Name the blood parasite species.
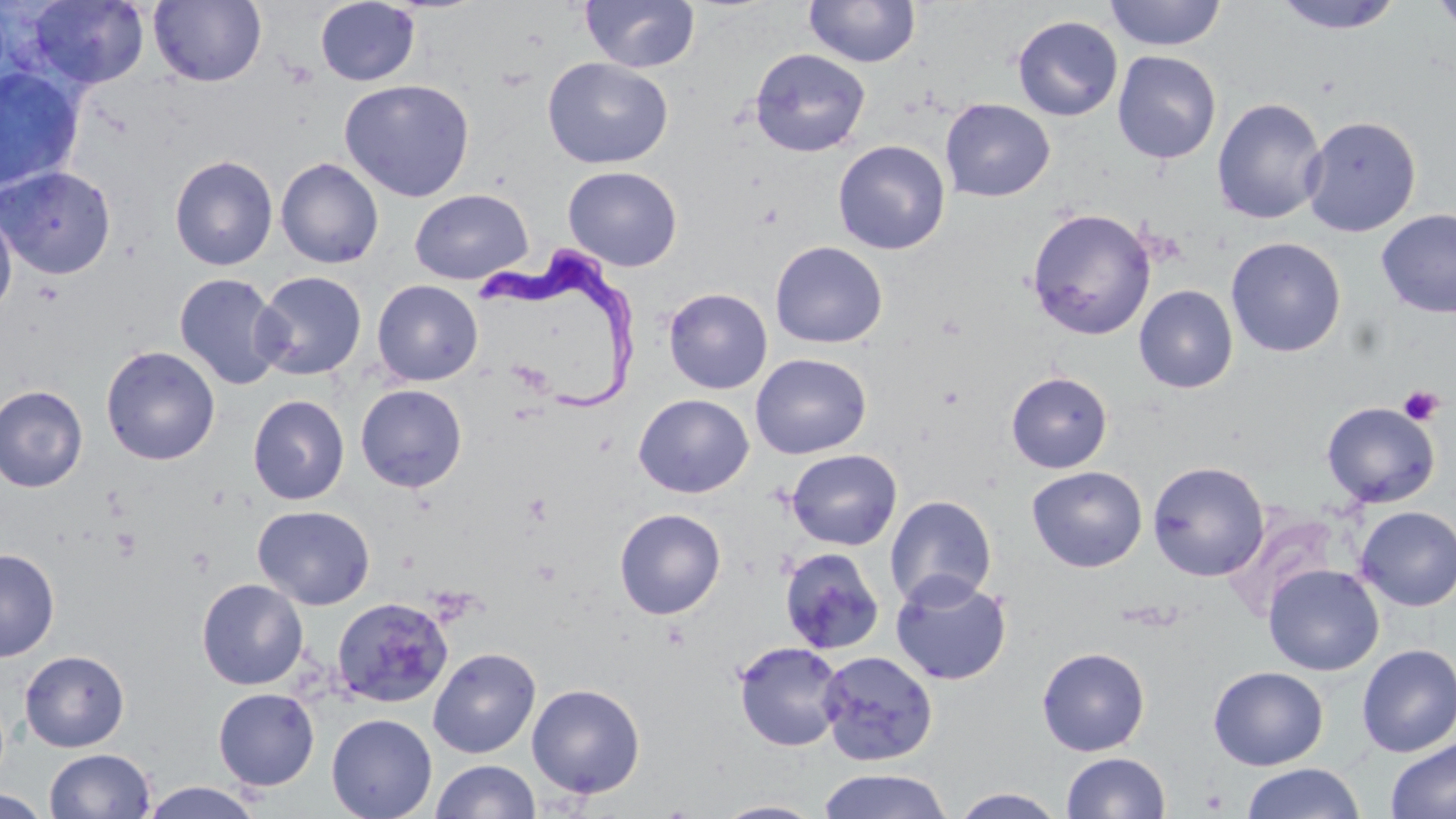
Trypanosoma brucei.

Approximate bounding boxes as (x1, y1, x2, y2) in pixels. Platelet locations: (1397, 384, 1444, 426), (110, 527, 143, 561), (1201, 787, 1229, 813). Uninfected red blood cell locations: (26, 0, 151, 90), (148, 0, 266, 87), (315, 0, 420, 87), (580, 0, 700, 73), (1105, 0, 1226, 51), (1273, 0, 1406, 35), (1431, 0, 1456, 37), (803, 1, 920, 68), (1012, 15, 1123, 121), (749, 47, 871, 158), (1112, 50, 1222, 164), (542, 57, 673, 169), (0, 66, 83, 194), (339, 78, 476, 202), (1212, 96, 1327, 225), (940, 98, 1055, 202), (1301, 116, 1420, 237), (832, 139, 950, 255), (169, 154, 278, 271), (275, 157, 384, 269), (0, 166, 116, 279), (563, 166, 683, 271), (410, 188, 533, 285), (0, 203, 17, 317), (1026, 207, 1157, 340), (1376, 209, 1456, 318), (1226, 237, 1346, 357), (770, 241, 888, 348), (253, 270, 367, 380), (174, 272, 288, 391), (372, 279, 483, 386), (1134, 285, 1238, 394), (663, 287, 773, 394), (101, 345, 220, 465), (750, 353, 871, 458), (1005, 371, 1113, 473), (355, 384, 468, 493), (0, 385, 88, 492), (633, 393, 754, 498), (247, 394, 350, 506), (1321, 401, 1440, 508), (786, 449, 903, 550), (1148, 461, 1269, 581), (1027, 466, 1148, 572), (885, 494, 997, 609), (252, 504, 376, 610), (1355, 506, 1456, 610), (614, 508, 726, 619), (778, 547, 885, 655), (0, 548, 60, 662), (1264, 564, 1384, 676), (890, 573, 1012, 686), (196, 578, 309, 690), (331, 596, 454, 709), (732, 640, 846, 752), (1356, 644, 1456, 758), (428, 646, 541, 758), (1037, 647, 1150, 756), (20, 649, 129, 752), (817, 649, 939, 766), (1208, 666, 1328, 770), (526, 683, 646, 799), (213, 687, 320, 790), (326, 713, 437, 819), (1385, 737, 1456, 819), (44, 748, 156, 819), (1061, 751, 1171, 818), (430, 759, 541, 819), (1241, 763, 1366, 819), (817, 768, 954, 819), (139, 781, 264, 819), (950, 787, 1067, 818), (0, 790, 50, 817), (712, 799, 827, 818). Trypanosoma brucei locations: (471, 241, 642, 412). Optical microscopy. May-Grünwald-Giemsa stain. 1000x magnification. Image is 1456×819 pixels. One field of a larger specimen. Thin blood smear.